Report the malaria status of this cell.
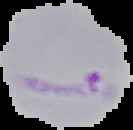

It is parasitized.

preparation = thin blood film
image size = 133×130 pixels
image type = cell region segmented out of the field of view; surrounding area masked to black